Give the position of every leukocyte visible.
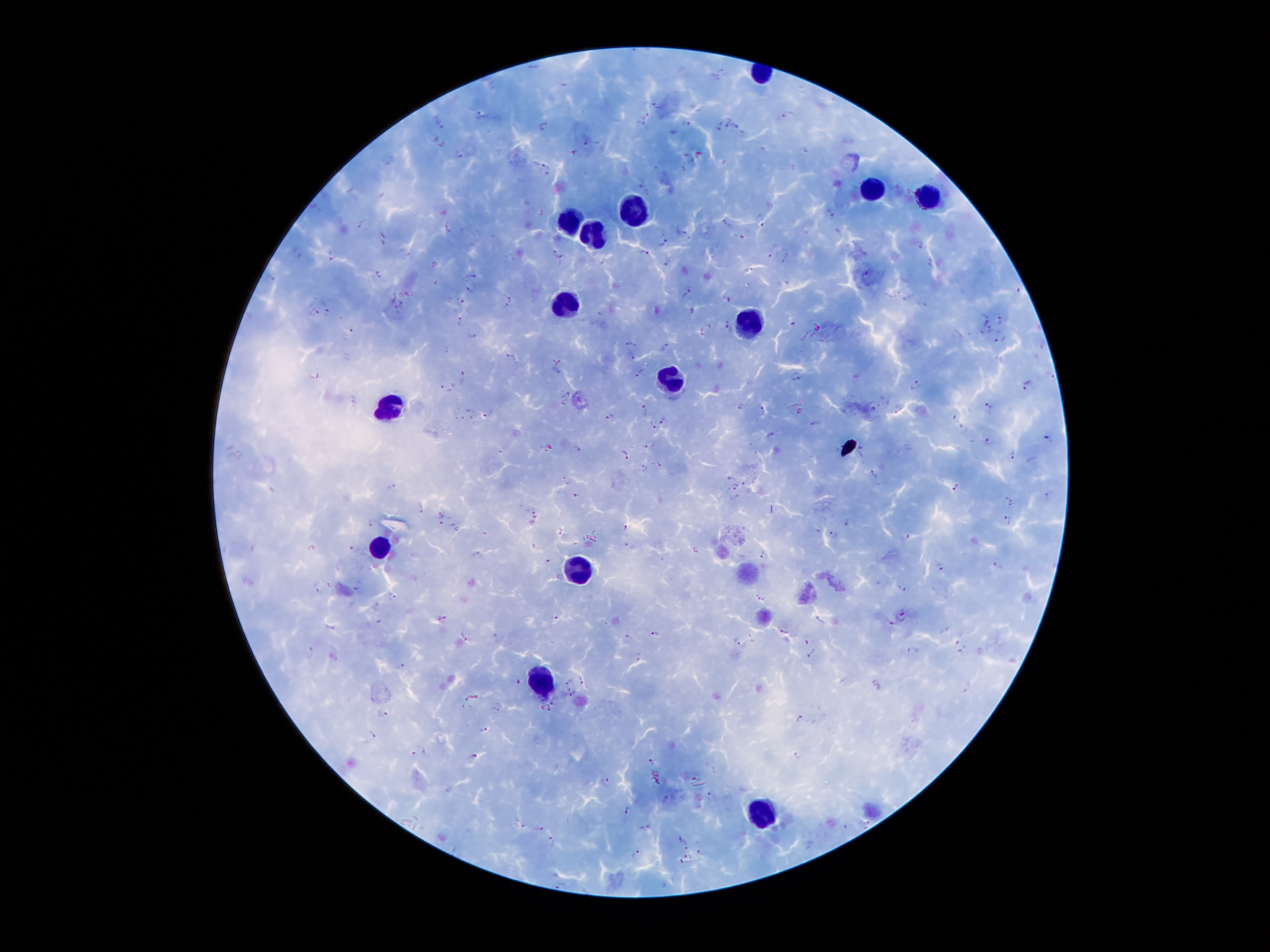
Approximate centers as {x, y} in pixels.
Leukocytes: {876, 191}, {925, 197}, {635, 200}, {576, 221}, {590, 234}, {565, 302}, {752, 326}, {672, 381}, {392, 408}, {379, 548}, {581, 568}, {542, 685}, {759, 808}.

Summary:
  - Malaria parasite locations: {723, 73}, {656, 105}, {478, 114}, {646, 116}, {782, 116}, {439, 124}, {642, 124}, {687, 124}, {543, 125}, {723, 125}, {735, 126}, {720, 130}, {585, 144}, {803, 149}, {459, 153}, {572, 154}, {544, 165}, {547, 174}, {642, 184}, {830, 214}, {760, 221}, {362, 222}, {728, 224}, {448, 225}, {745, 235}, {660, 238}, {920, 245}, {772, 250}, {554, 251}, {297, 253}, {643, 253}, {332, 256}, {561, 257}, {666, 261}, {750, 270}, {868, 272}, {377, 274}, {473, 274}, {270, 279}, {783, 280}, {469, 289}, {685, 293}, {726, 297}, {510, 298}, {909, 298}, {461, 299}, {926, 305}, {507, 306}, {328, 308}, {691, 311}, {313, 313}, {461, 318}, {998, 319}, {984, 322}, {725, 324}, {989, 328}, {702, 329}, {350, 330}, {473, 336}, {1000, 338}, {630, 342}, {667, 346}, {510, 354}, {634, 355}, {557, 368}, {463, 372}, {640, 373}, {314, 374}, {798, 376}, {1027, 384}, {917, 386}, {446, 388}, {564, 393}, {987, 404}, {565, 405}, {740, 406}, {761, 406}, {872, 407}, {898, 409}, {646, 411}, {488, 412}, {608, 416}, {663, 419}, {958, 421}, {815, 423}, {652, 426}, {772, 433}, {1049, 437}, {988, 442}, {577, 447}, {624, 455}, {1012, 455}, {646, 468}, {874, 473}, {730, 479}, {566, 480}, {393, 486}, {954, 486}, {737, 487}, {576, 494}, {1047, 496}, {732, 497}, {1009, 499}, {422, 508}, {534, 512}, {441, 513}, {1006, 517}, {440, 522}, {849, 522}, {373, 524}, {624, 526}, {560, 532}, {836, 535}, {630, 545}, {351, 550}, {475, 554}, {763, 554}, {548, 558}, {940, 564}, {996, 564}, {358, 584}, {903, 585}, {392, 595}, {760, 596}, {377, 606}, {903, 615}, {556, 616}, {444, 618}, {818, 618}, {890, 621}, {783, 631}, {653, 633}, {466, 634}, {630, 637}, {738, 641}, {961, 646}, {309, 650}, {915, 650}, {811, 653}, {637, 656}, {401, 666}, {581, 679}, {518, 681}, {570, 681}, {968, 687}, {571, 692}, {553, 699}, {466, 706}, {498, 706}, {383, 714}, {800, 719}, {483, 728}, {371, 734}, {419, 750}, {474, 755}, {798, 756}, {652, 760}, {606, 779}, {707, 794}, {626, 808}, {867, 824}, {523, 825}, {540, 827}, {647, 828}, {681, 840}, {554, 842}, {685, 847}, {700, 852}, {636, 854}, {688, 856}, {682, 860}
  - Preparation: thick blood film
  - Patient malaria status: infected with Plasmodium falciparum
  - Field of view: one from this slide
  - Capture: smartphone camera through the microscope eyepiece
  - Magnification: 100x
  - Image size: 1270×952 pixels
  - Stain: Giemsa